Comment on the morphology of the erythrocytes.
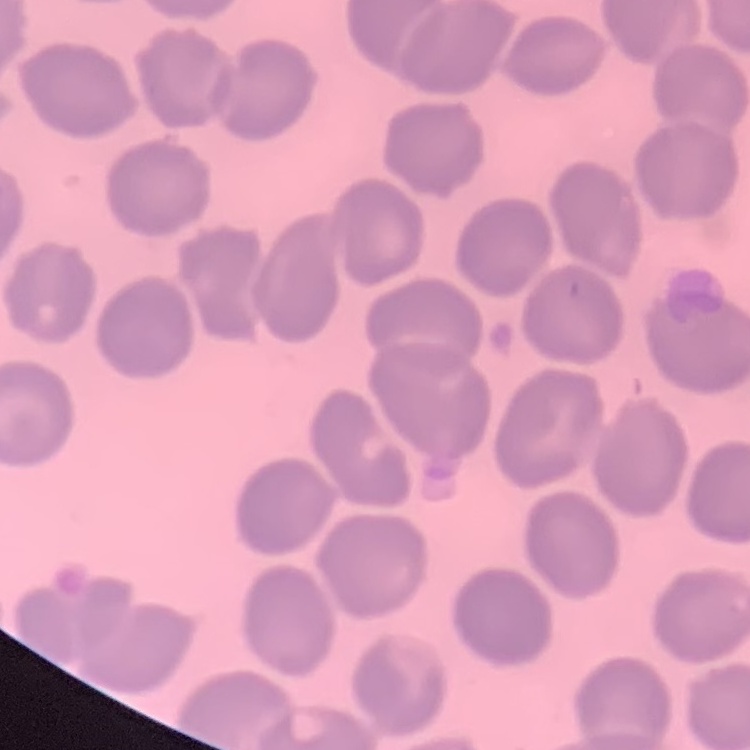

They show no rouleaux formation.

Stained with either Field's or Giemsa. Thin peripheral smear. Square crop of a larger photomicrograph.